Locate every Plasmodium vivax-infected red blood cell.
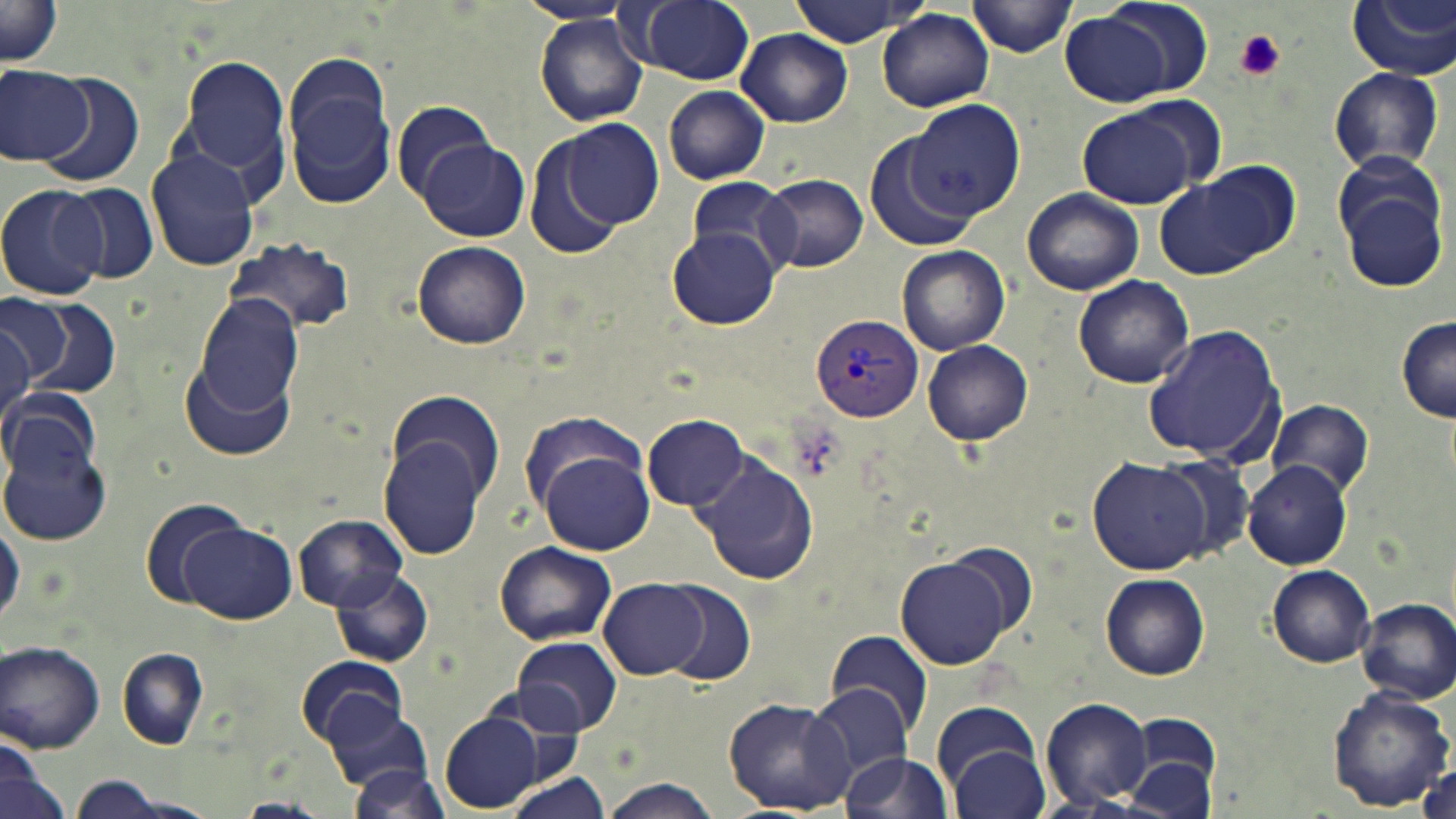

Approximate bounding boxes as (x1, y1, x2, y2) in pixels.
Plasmodium vivax-infected red blood cells: (810, 313, 924, 420).

Platelet locations: (1232, 29, 1286, 82). Uninfected red blood cell locations: (631, 0, 755, 85), (970, 0, 1078, 57), (1347, 0, 1456, 81), (788, 1, 925, 47), (1, 3, 64, 69), (1059, 8, 1191, 108), (878, 10, 994, 111), (533, 14, 649, 126), (737, 28, 853, 127), (278, 52, 396, 207), (178, 56, 291, 179), (0, 64, 94, 165), (1326, 66, 1445, 174), (28, 70, 143, 185), (663, 86, 771, 184), (901, 99, 1028, 230), (392, 102, 497, 203), (1077, 107, 1202, 210), (560, 118, 665, 230), (522, 135, 627, 261), (865, 135, 976, 254), (416, 140, 530, 242), (145, 148, 261, 272), (1198, 161, 1300, 259), (1155, 171, 1283, 281), (1333, 171, 1451, 294), (758, 174, 868, 273), (681, 178, 797, 271), (0, 183, 109, 301), (61, 184, 159, 284), (1022, 186, 1145, 295), (667, 227, 782, 330), (222, 236, 357, 335), (412, 241, 529, 349), (896, 245, 1010, 355), (1073, 275, 1194, 389), (8, 293, 119, 402), (194, 296, 304, 419), (0, 297, 64, 387), (1397, 314, 1456, 423), (0, 322, 35, 438), (1141, 323, 1285, 467), (922, 340, 1033, 446), (180, 359, 294, 461), (0, 386, 99, 488), (385, 390, 503, 503), (1267, 398, 1375, 496), (520, 410, 654, 519), (642, 412, 750, 511), (2, 428, 112, 548), (378, 435, 488, 560), (538, 449, 656, 556), (693, 453, 818, 587), (1153, 454, 1258, 565), (1087, 458, 1210, 575), (1243, 462, 1353, 569), (139, 497, 248, 606), (294, 515, 409, 611), (0, 518, 24, 630), (178, 520, 297, 625), (493, 541, 617, 646), (897, 555, 1018, 671), (1266, 565, 1376, 667), (328, 567, 433, 668), (1100, 573, 1209, 680), (599, 579, 709, 679), (654, 581, 756, 686), (1355, 599, 1456, 703), (825, 629, 934, 736), (512, 637, 621, 735), (2, 642, 105, 753), (116, 651, 209, 749), (297, 652, 407, 745), (808, 684, 918, 782), (1326, 684, 1454, 812), (1041, 696, 1156, 809), (320, 697, 434, 797), (723, 697, 856, 814), (932, 700, 1043, 794), (439, 711, 547, 810), (1125, 714, 1222, 817), (948, 745, 1049, 819), (1, 750, 69, 819), (839, 753, 954, 819), (1414, 753, 1456, 819), (345, 762, 456, 816), (506, 772, 612, 818), (63, 776, 197, 818), (599, 779, 723, 818), (230, 797, 330, 818). Slide-level diagnosis: Plasmodium vivax. Captured at 1000x magnification. May-Grünwald-Giemsa-stained preparation. Thin blood smear. Image is 1456×819 pixels. Optical microscopy. Single field of view.